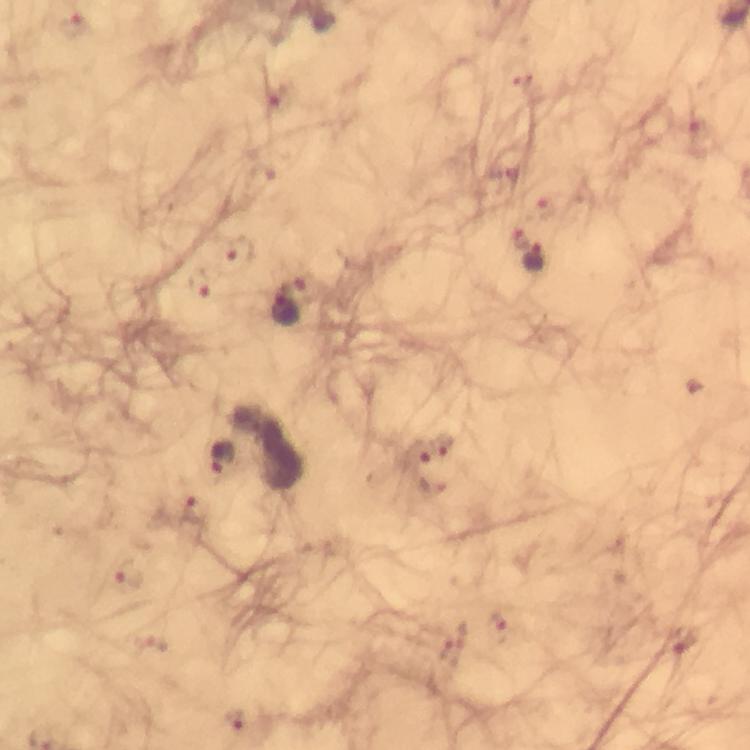
context = from a diagnostic examination for malaria
Plasmodium parasite locations = approximate centers as [x, y] in pixels: [73, 26], [524, 84], [276, 93], [695, 132], [545, 207], [518, 239], [240, 251], [535, 259], [200, 283], [287, 312], [445, 447], [417, 453], [224, 458], [195, 512], [128, 574], [498, 625], [681, 643], [448, 645], [236, 719]
capture = smartphone camera through the microscope
stain = Giemsa
cropped from = a single field of view
image size = 750×750 pixels
preparation = thick blood smear
immersion oil = used
magnification = 100x